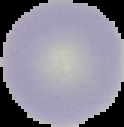

Summary:
  - Image size: 124×127 pixels
  - Image type: segmented cell region with the area outside set to black
  - Preparation: thin blood smear
  - Malaria status: uninfected